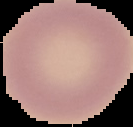

image size = 133×127 pixels
image type = segmented cell region with the area outside set to black
result = negative for Plasmodium parasites
preparation = thin blood film